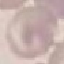
{
  "malaria_status": "uninfected",
  "stain": "Giemsa",
  "capture": "smartphone through the microscope eyepiece",
  "image_type": "automatically extracted cell patch, resized to 64 × 64 pixels",
  "preparation": "thin blood film"
}